Outline each blood parasite and name the species.
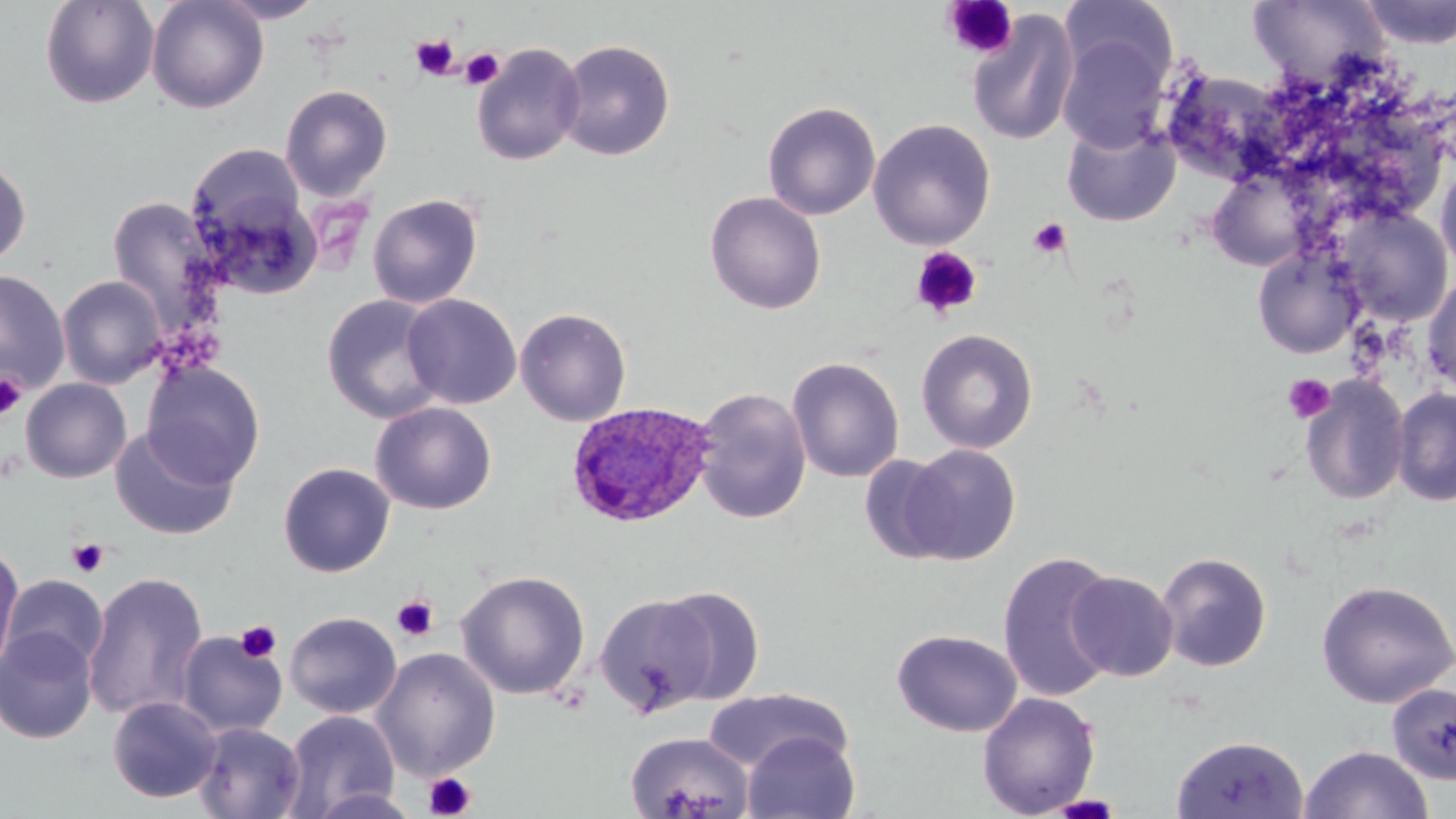
Approximate bounding boxes as [x1, y1, x2, y2] in pixels.
Plasmodium ovale-infected red blood cells: [567, 401, 717, 528].
No Plasmodium falciparum, Plasmodium malariae, Plasmodium vivax, Babesia divergens, or Trypanosoma brucei observed.

slide_level_diagnosis: Plasmodium ovale
magnification: 1000x
platelet_locations_subset: 'approximate bounding boxes as [x1, y1, x2, y2] in pixels: [942, 0, 1019, 60], [411, 35, 459, 80], [460, 48, 505, 90], [1028, 218, 1072, 259], [911, 246, 983, 319], [0, 372, 27, 420], [1283, 374, 1335, 423], [67, 538, 110, 577], [391, 595, 438, 642], [235, 620, 282, 663], [424, 772, 477, 818], [1049, 794, 1124, 817]'
image_size: 1456×819 pixels
preparation: thin blood film
uninfected_red_blood_cell_locations_subset: 'approximate bounding boxes as [x1, y1, x2, y2] in pixels: [40, 0, 160, 109], [146, 0, 269, 113], [211, 0, 329, 23], [1358, 0, 1456, 49], [1060, 1, 1177, 94], [1248, 1, 1389, 87], [966, 9, 1080, 146], [1058, 32, 1170, 153], [555, 39, 675, 161], [471, 42, 586, 166], [1161, 69, 1293, 184], [280, 84, 393, 199], [762, 101, 881, 221], [1062, 120, 1180, 227], [186, 144, 312, 261], [0, 156, 32, 270], [1435, 159, 1456, 275], [1206, 169, 1311, 270], [192, 184, 323, 301], [705, 191, 826, 315], [367, 193, 483, 309], [107, 197, 215, 322], [1335, 207, 1453, 325], [1253, 246, 1363, 359], [0, 269, 70, 394], [1422, 273, 1456, 397], [57, 275, 167, 389], [321, 294, 447, 424], [402, 294, 522, 409], [515, 307, 632, 427], [916, 328, 1039, 453], [787, 356, 905, 483], [141, 361, 265, 488], [1300, 375, 1410, 506], [21, 378, 132, 483], [693, 387, 811, 524], [1391, 388, 1456, 506], [370, 401, 497, 515], [109, 427, 238, 541], [900, 443, 1021, 565], [859, 454, 960, 564], [278, 462, 395, 577], [0, 543, 23, 677], [997, 550, 1121, 703], [1157, 551, 1272, 672], [456, 569, 591, 700], [82, 570, 210, 723], [1065, 570, 1179, 682], [3, 574, 108, 676], [1316, 579, 1456, 708], [652, 585, 766, 706], [594, 593, 718, 717], [284, 611, 402, 719], [1, 626, 99, 743], [891, 628, 1023, 737], [175, 630, 288, 738], [372, 648, 501, 780], [1387, 683, 1456, 785], [703, 687, 855, 774], [977, 692, 1101, 818], [107, 696, 221, 803], [283, 710, 399, 817], [192, 721, 306, 819], [625, 731, 755, 818], [741, 731, 860, 818], [1170, 735, 1310, 819], [1298, 745, 1434, 819], [307, 788, 424, 819]'
modality: light microscopy
stain: May-Grünwald-Giemsa
field_of_view: one of a larger specimen